Report the malaria status of this cell.
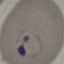

It is parasitized.

{
  "preparation": "thin smear",
  "capture": "smartphone camera at the microscope eyepiece",
  "image_type": "automatically extracted cell patch, resized to 64 × 64 pixels",
  "stain": "Giemsa"
}